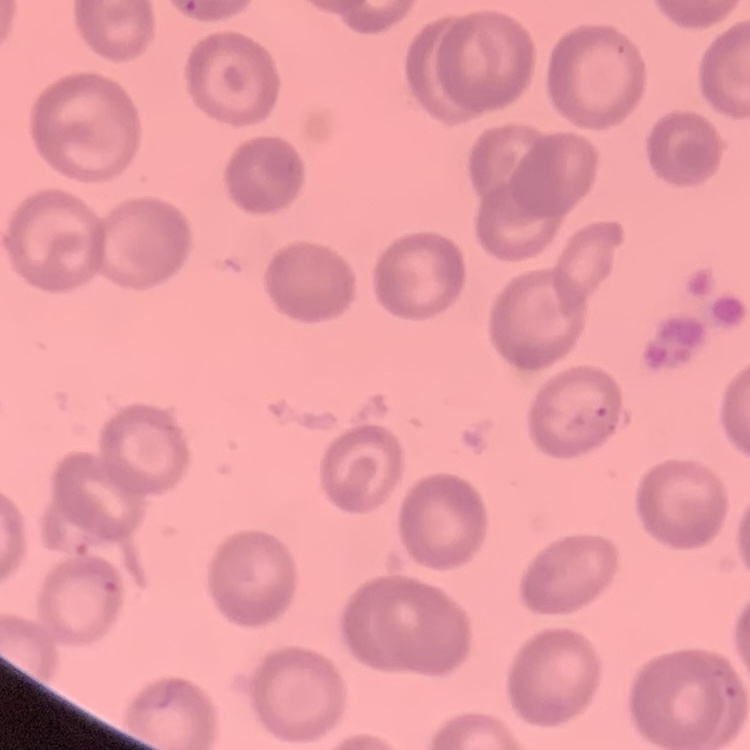
erythrocyte morphology = no rouleaux formation
stain = Field's or Giemsa
preparation = thin blood smear
image type = square crop of a larger photomicrograph